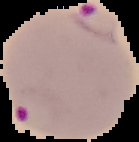
image type = segmented cell region on a black background
preparation = thin blood film
malaria status = parasitized
image size = 139×142 pixels